Report the malaria status of this cell.
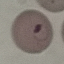
It is parasitized.

Summary:
  - Stain: Giemsa
  - Capture: smartphone through the microscope eyepiece
  - Preparation: thin smear
  - Image type: cell patch, automatically extracted from a larger field of view and resized to 64 × 64 pixels